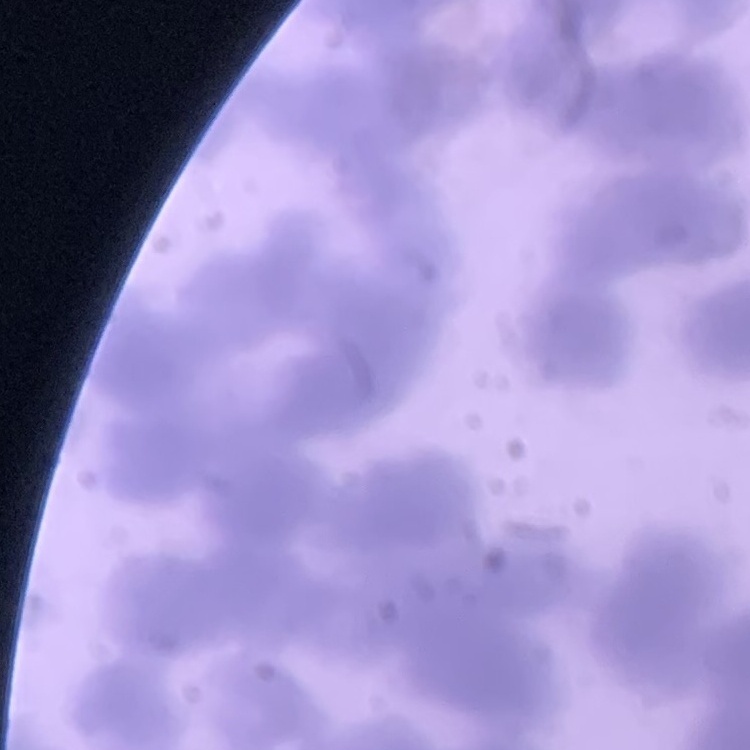
Summary:
  - Red blood cell morphology: rouleaux formation
  - Image type: one tile cut from a larger photomicrograph
  - Preparation: thin blood film
  - Stain: Field's or Giemsa